Identify the parasite.
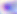

Toxoplasma gondii.

400x magnification. Micrograph.